Give the position of every leukocyte visible.
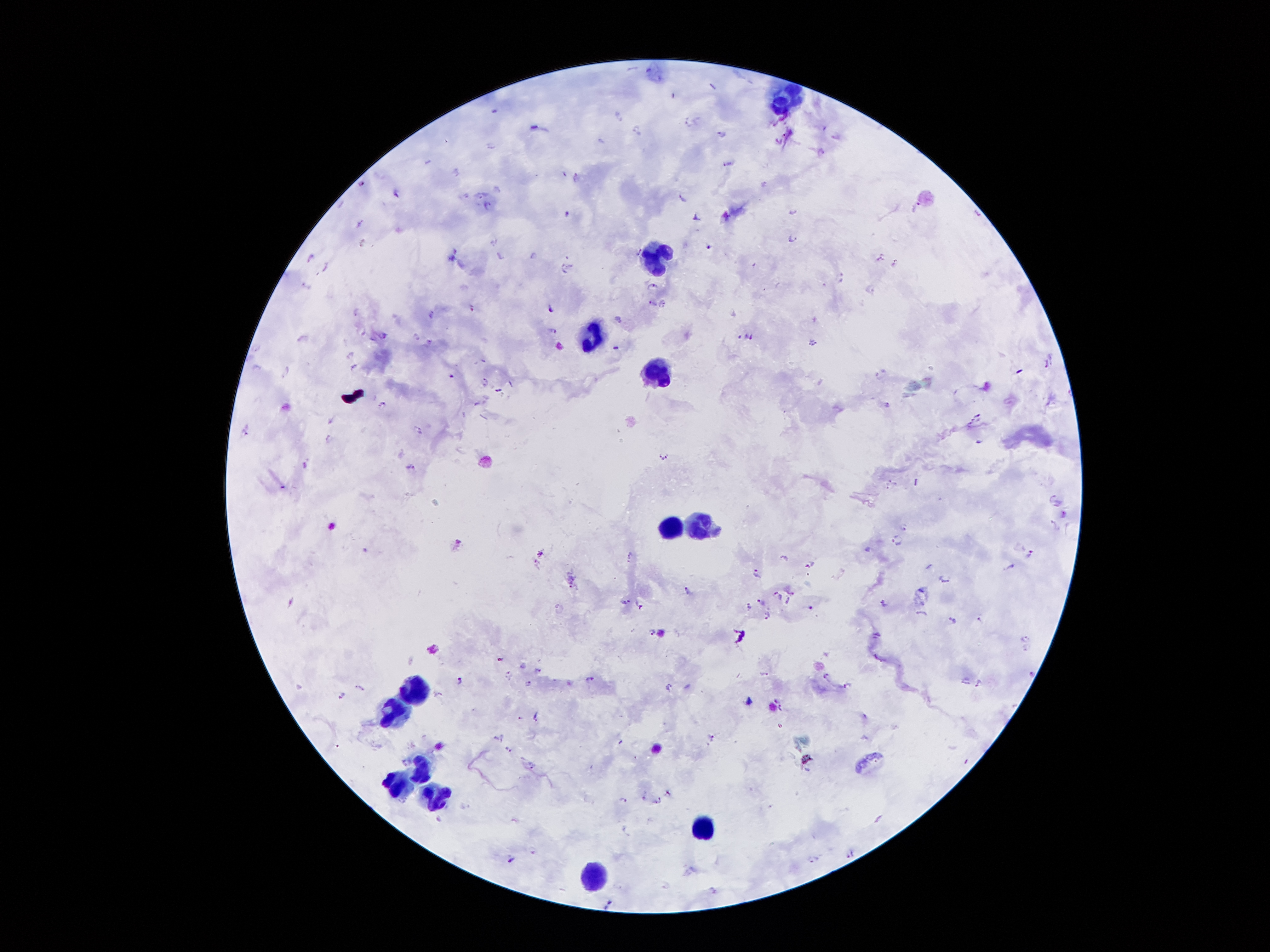
Approximate object centers, in pixels from the top-left corner.
Leukocytes: (x=787, y=97), (x=655, y=256), (x=594, y=336), (x=656, y=373), (x=699, y=526), (x=671, y=528), (x=421, y=691), (x=394, y=709), (x=421, y=767), (x=395, y=785), (x=437, y=795), (x=701, y=827), (x=593, y=875).

Summary:
  - Plasmodium parasite locations: (x=617, y=114), (x=689, y=123), (x=538, y=128), (x=639, y=132), (x=722, y=135), (x=601, y=141), (x=820, y=152), (x=728, y=163), (x=456, y=171), (x=576, y=176), (x=361, y=183), (x=396, y=193), (x=682, y=195), (x=487, y=205), (x=794, y=210), (x=568, y=215), (x=726, y=215), (x=695, y=217), (x=359, y=223), (x=793, y=237), (x=363, y=243), (x=708, y=243), (x=452, y=253), (x=533, y=255), (x=310, y=258), (x=880, y=258), (x=894, y=262), (x=325, y=268), (x=566, y=268), (x=839, y=278), (x=308, y=286), (x=652, y=286), (x=871, y=289), (x=651, y=303), (x=663, y=303), (x=471, y=308), (x=550, y=309), (x=357, y=311), (x=430, y=314), (x=618, y=318), (x=554, y=330), (x=383, y=333), (x=416, y=336), (x=748, y=337), (x=430, y=341), (x=811, y=342), (x=616, y=347), (x=255, y=348), (x=350, y=354), (x=1053, y=359), (x=1044, y=364), (x=354, y=367), (x=286, y=370), (x=485, y=380), (x=498, y=389), (x=382, y=405), (x=887, y=405), (x=978, y=416), (x=331, y=420), (x=970, y=424), (x=245, y=430), (x=417, y=430), (x=328, y=438), (x=977, y=441), (x=664, y=455), (x=304, y=465), (x=410, y=466), (x=894, y=481), (x=887, y=489), (x=1053, y=497), (x=1052, y=523), (x=904, y=526), (x=897, y=540), (x=457, y=542), (x=869, y=550), (x=541, y=553), (x=1029, y=554), (x=629, y=555), (x=784, y=557), (x=535, y=561), (x=809, y=564), (x=1013, y=565), (x=756, y=572), (x=945, y=578), (x=571, y=582), (x=687, y=590), (x=776, y=593), (x=792, y=593), (x=781, y=597), (x=626, y=600), (x=788, y=600), (x=760, y=601), (x=884, y=603), (x=639, y=605), (x=749, y=606), (x=812, y=607), (x=767, y=615), (x=952, y=619), (x=980, y=619), (x=651, y=632), (x=876, y=634), (x=1025, y=638), (x=501, y=660), (x=537, y=670), (x=1031, y=671), (x=764, y=673), (x=506, y=674), (x=826, y=675), (x=966, y=678), (x=589, y=679), (x=459, y=680), (x=980, y=681), (x=530, y=684), (x=846, y=685), (x=362, y=686), (x=667, y=686), (x=342, y=695), (x=777, y=699), (x=780, y=708), (x=520, y=717), (x=536, y=717), (x=501, y=736), (x=710, y=737), (x=620, y=742), (x=508, y=747), (x=533, y=765), (x=669, y=793), (x=642, y=795), (x=624, y=800), (x=656, y=800), (x=438, y=818), (x=849, y=853), (x=812, y=857), (x=510, y=860), (x=713, y=890), (x=609, y=901)
  - Image size: 1270×952 pixels
  - Magnification: 100x
  - Patient malaria status: positive for Plasmodium falciparum
  - Preparation: thick peripheral-blood smear
  - Field of view: one from this slide
  - Stain: Giemsa
  - Capture: smartphone camera through the microscope eyepiece